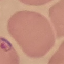

Summary:
  - Result: malaria parasites identified
  - Stain: Giemsa
  - Preparation: thin blood film
  - Capture: smartphone camera at the microscope eyepiece
  - Image type: automatically extracted cell patch, resized to 64 × 64 pixels